Identify the parasite.
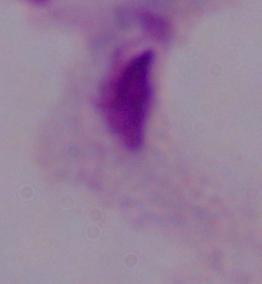
This is a trichomonad.

Summary:
  - Magnification: 1000x
  - Modality: micrograph